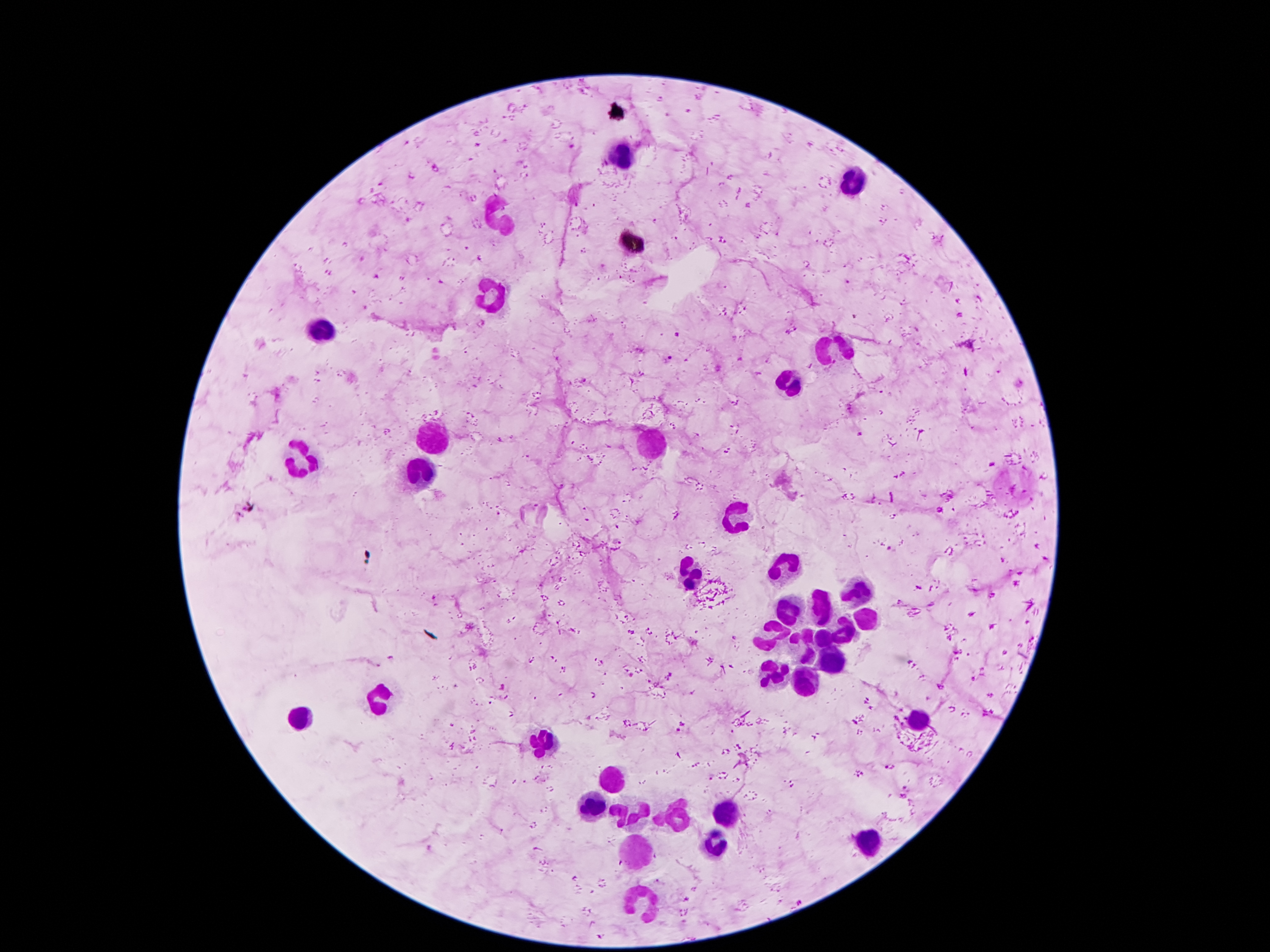

Approximate centers as [x, y] in pixels.
Summary:
  - Plasmodium parasite locations: [677, 334], [669, 358], [244, 511], [436, 600], [682, 727], [889, 766]
  - Leukocyte locations: [623, 155], [850, 182], [493, 216], [498, 298], [323, 334], [829, 354], [791, 382], [437, 440], [645, 440], [302, 463], [423, 468], [734, 518], [782, 566], [858, 593], [822, 606], [793, 611], [865, 622], [845, 627], [768, 631], [824, 640], [802, 649], [836, 659], [774, 677], [809, 684], [378, 700], [303, 718], [920, 722], [538, 742], [611, 779], [595, 806], [629, 811], [723, 815], [673, 818], [716, 842], [636, 843], [872, 843], [645, 902]
  - Preparation: thick blood smear
  - Capture: smartphone through the microscope eyepiece
  - Patient malaria status: infected with Plasmodium falciparum
  - Magnification: 100x
  - Field of view: one from this slide
  - Image size: 1270×952 pixels
  - Stain: Giemsa